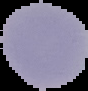
Summary:
  - Image size: 88×91 pixels
  - Preparation: thin blood smear
  - Malaria status: parasitized
  - Image type: cell region segmented out of the field of view; surrounding area masked to black